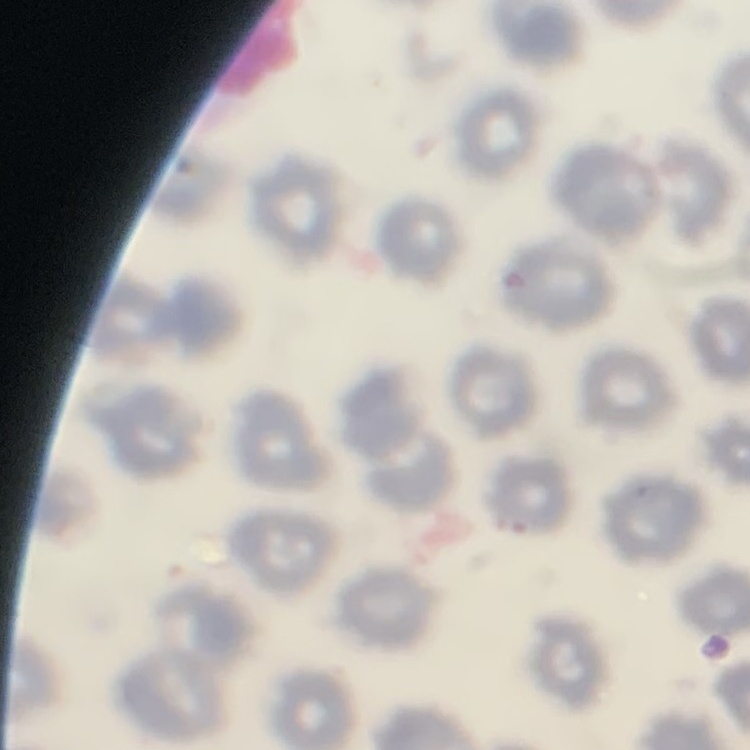

erythrocyte morphology = no rouleaux formation
image type = square crop of a larger photomicrograph
preparation = thin blood smear
stain = Field's or Giemsa